Locate every blood parasite and identify its species.
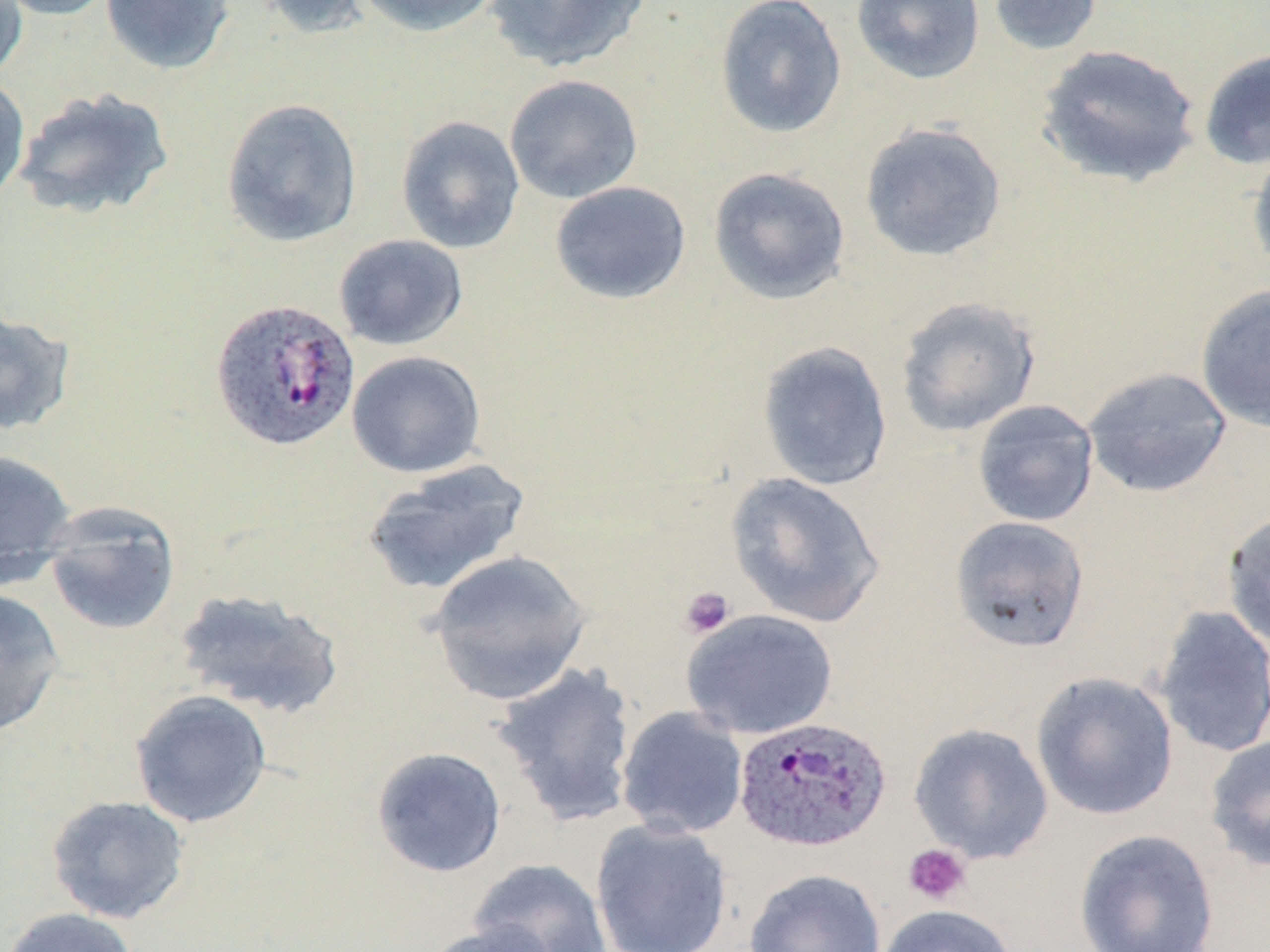
Approximate bounding boxes as (x1, y1, x2, y2) in pixels.
Plasmodium ovale-infected red blood cells: (209, 297, 360, 451), (734, 716, 892, 854).
No Plasmodium falciparum, Plasmodium malariae, Plasmodium vivax, Babesia divergens, or Trypanosoma brucei observed.

Uninfected red blood cell locations: (0, 0, 118, 21), (0, 0, 29, 84), (99, 0, 236, 75), (247, 0, 376, 39), (354, 0, 501, 37), (482, 0, 652, 73), (715, 0, 847, 139), (851, 0, 986, 85), (987, 0, 1103, 56), (1035, 43, 1202, 188), (1198, 48, 1270, 171), (0, 73, 31, 205), (504, 73, 644, 204), (11, 87, 176, 220), (221, 97, 363, 248), (395, 115, 525, 255), (858, 121, 1007, 263), (1247, 140, 1270, 280), (708, 166, 851, 305), (550, 181, 692, 304), (334, 234, 468, 350), (1195, 283, 1270, 434), (894, 296, 1042, 438), (0, 308, 76, 437), (757, 340, 893, 491), (347, 350, 487, 478), (1082, 366, 1233, 498), (971, 400, 1100, 527), (0, 449, 78, 586), (360, 459, 531, 597), (724, 472, 886, 628), (41, 505, 181, 637), (1221, 508, 1270, 651), (949, 515, 1090, 652), (426, 549, 593, 705), (0, 587, 66, 738), (173, 587, 346, 720), (1151, 606, 1270, 759), (681, 609, 839, 740), (492, 663, 639, 826), (1030, 671, 1179, 821), (130, 689, 273, 828), (616, 706, 749, 840), (908, 723, 1054, 864), (1203, 733, 1270, 873), (371, 746, 507, 878), (46, 795, 191, 924), (590, 819, 734, 952), (1074, 829, 1220, 952), (896, 841, 978, 914), (469, 858, 612, 952), (744, 868, 886, 952), (875, 904, 1018, 952), (0, 907, 141, 952), (422, 921, 562, 952). Platelet locations: (679, 586, 735, 639), (902, 843, 971, 906). Slide-level diagnosis: Plasmodium ovale. Light microscopy. Single field of view. 1000x magnification. Thin blood film. Image is 1270×952 pixels. May-Grünwald-Giemsa-stained preparation.